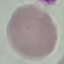

Summary:
  - Malaria status: uninfected
  - Capture: smartphone through the microscope eyepiece
  - Preparation: thin blood smear
  - Image type: cell patch, automatically extracted from a larger field of view and resized to 64 × 64 pixels
  - Stain: Giemsa